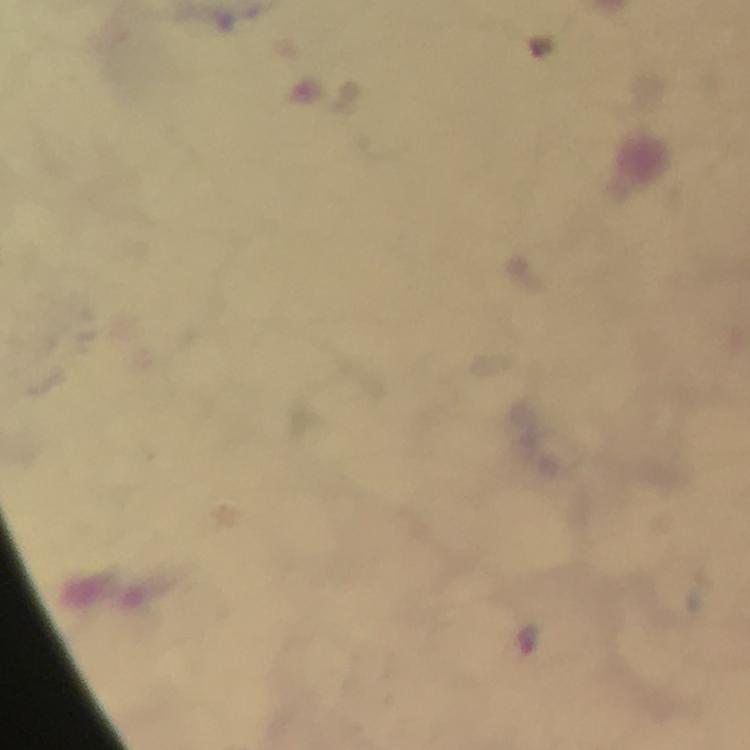
image_size: 750×750 pixels
malaria_parasite_locations: 'approximate centers as {x, y} in pixels: {528, 636}'
context: from a diagnostic examination for malaria
immersion_oil: applied
cropped_from: one field of view
stain: Giemsa
magnification: 100x
preparation: thick smear
capture: smartphone camera through the microscope